Assess this cell for malaria.
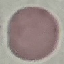
It is uninfected.

Acquired by smartphone through the microscope eyepiece. Automatically extracted cell patch, resized to 64 × 64 pixels. Thin smear of blood. Giemsa stain.